Outline each blood parasite and name the species.
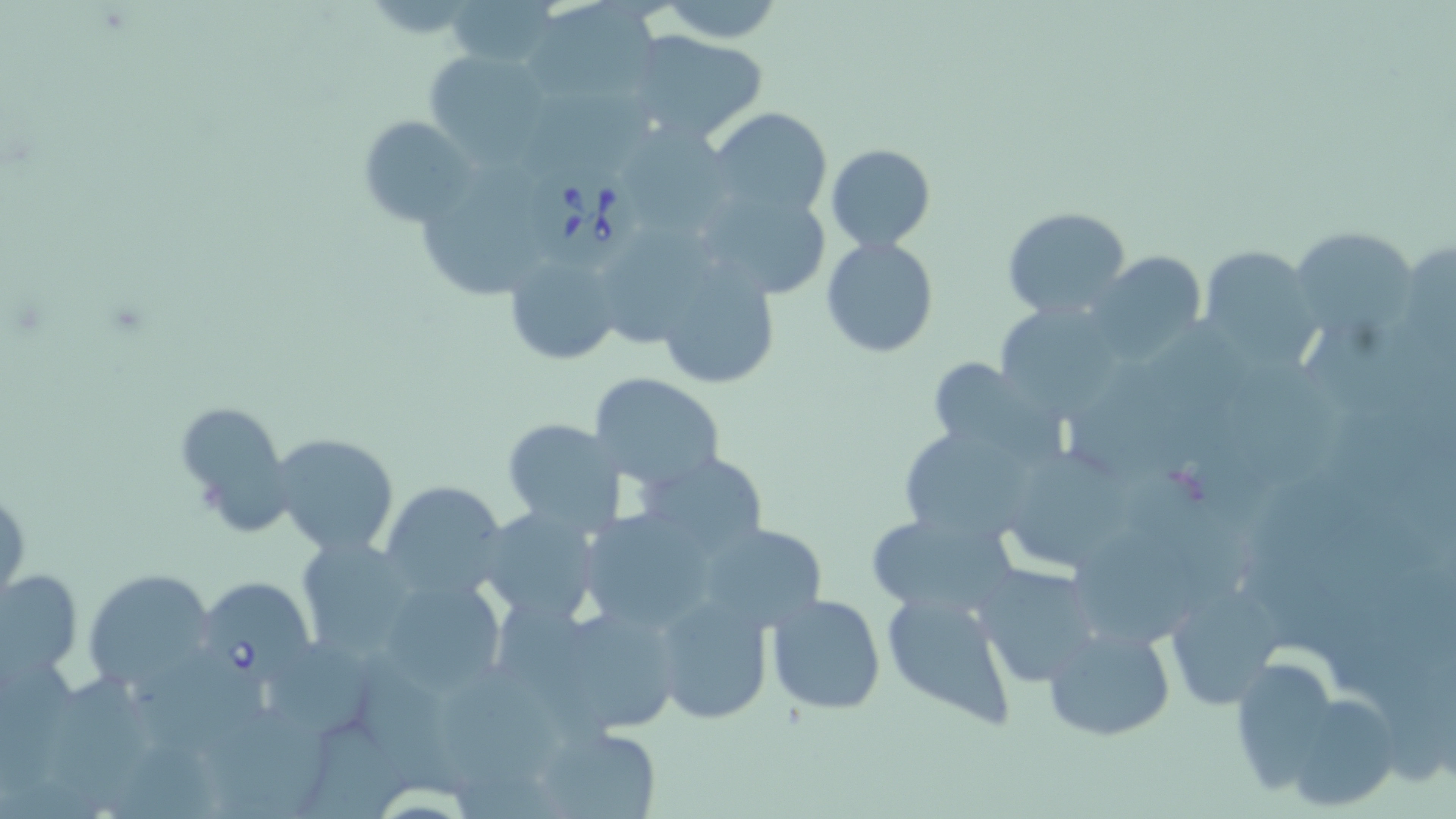
Approximate bounding boxes as named x1/y1/x2/y2 corners in pixels.
Babesia divergens-infected red blood cells: (x1=525, y1=162, x2=645, y2=272), (x1=196, y1=576, x2=317, y2=681).
No Plasmodium falciparum, Plasmodium ovale, Plasmodium malariae, Plasmodium vivax, or Trypanosoma brucei observed.

Uninfected red blood cell locations: (x1=445, y1=0, x2=557, y2=72), (x1=655, y1=1, x2=785, y2=44), (x1=528, y1=2, x2=663, y2=106), (x1=625, y1=29, x2=771, y2=146), (x1=425, y1=49, x2=552, y2=161), (x1=524, y1=91, x2=663, y2=173), (x1=709, y1=107, x2=834, y2=220), (x1=359, y1=114, x2=477, y2=225), (x1=613, y1=129, x2=736, y2=236), (x1=826, y1=143, x2=936, y2=252), (x1=425, y1=159, x2=536, y2=301), (x1=693, y1=182, x2=835, y2=301), (x1=1003, y1=206, x2=1133, y2=318), (x1=1291, y1=227, x2=1421, y2=340), (x1=599, y1=231, x2=720, y2=344), (x1=821, y1=236, x2=940, y2=356), (x1=1198, y1=247, x2=1324, y2=366), (x1=505, y1=248, x2=626, y2=366), (x1=1090, y1=251, x2=1209, y2=361), (x1=652, y1=260, x2=780, y2=390), (x1=994, y1=300, x2=1130, y2=417), (x1=1230, y1=355, x2=1344, y2=486), (x1=927, y1=357, x2=1052, y2=458), (x1=1067, y1=363, x2=1200, y2=482), (x1=589, y1=371, x2=726, y2=492), (x1=174, y1=400, x2=293, y2=530), (x1=501, y1=418, x2=625, y2=534), (x1=900, y1=422, x2=1034, y2=542), (x1=270, y1=430, x2=401, y2=558), (x1=640, y1=449, x2=771, y2=558), (x1=1017, y1=450, x2=1130, y2=569), (x1=380, y1=480, x2=509, y2=601), (x1=0, y1=484, x2=28, y2=604), (x1=473, y1=505, x2=605, y2=626), (x1=575, y1=506, x2=721, y2=633), (x1=862, y1=513, x2=1019, y2=618), (x1=699, y1=523, x2=827, y2=631), (x1=1076, y1=533, x2=1200, y2=643), (x1=295, y1=537, x2=418, y2=657), (x1=973, y1=563, x2=1101, y2=688), (x1=84, y1=567, x2=218, y2=692), (x1=2, y1=568, x2=82, y2=679), (x1=377, y1=573, x2=508, y2=696), (x1=1163, y1=582, x2=1286, y2=711), (x1=880, y1=586, x2=1019, y2=729), (x1=654, y1=592, x2=775, y2=726), (x1=766, y1=592, x2=886, y2=716), (x1=540, y1=602, x2=686, y2=736), (x1=1043, y1=622, x2=1176, y2=743), (x1=269, y1=643, x2=378, y2=741), (x1=150, y1=655, x2=268, y2=758), (x1=1229, y1=655, x2=1340, y2=791), (x1=436, y1=660, x2=566, y2=793), (x1=356, y1=662, x2=463, y2=794), (x1=53, y1=672, x2=154, y2=810), (x1=1276, y1=692, x2=1398, y2=813), (x1=210, y1=707, x2=327, y2=819), (x1=533, y1=724, x2=665, y2=819), (x1=304, y1=725, x2=412, y2=819). Slide-level diagnosis: Babesia divergens. Thin blood smear. May-Grünwald-Giemsa-stained preparation. Light microscopy. Captured at 1000x magnification. One field of a larger specimen. Image is 1456×819 pixels.